Name the parasite shown.
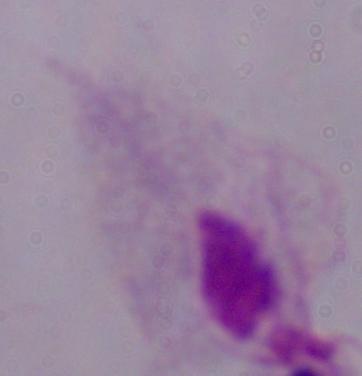
A trichomonad.

Captured at 1000x magnification. Photomicrograph.